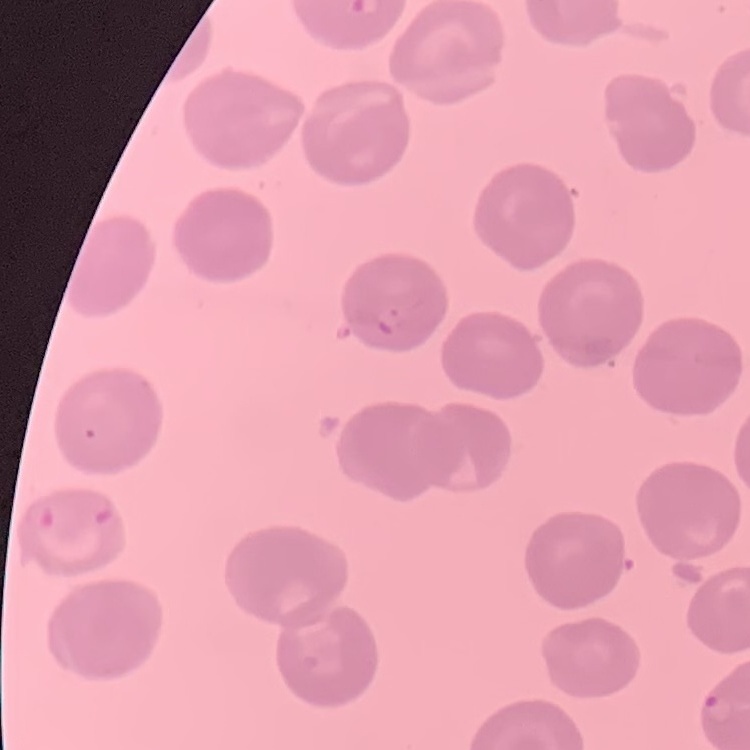 The erythrocytes show no rouleaux formation. Field's or Giemsa stain. Thin blood film. One tile cut from a larger photomicrograph.